Give the preparation type.
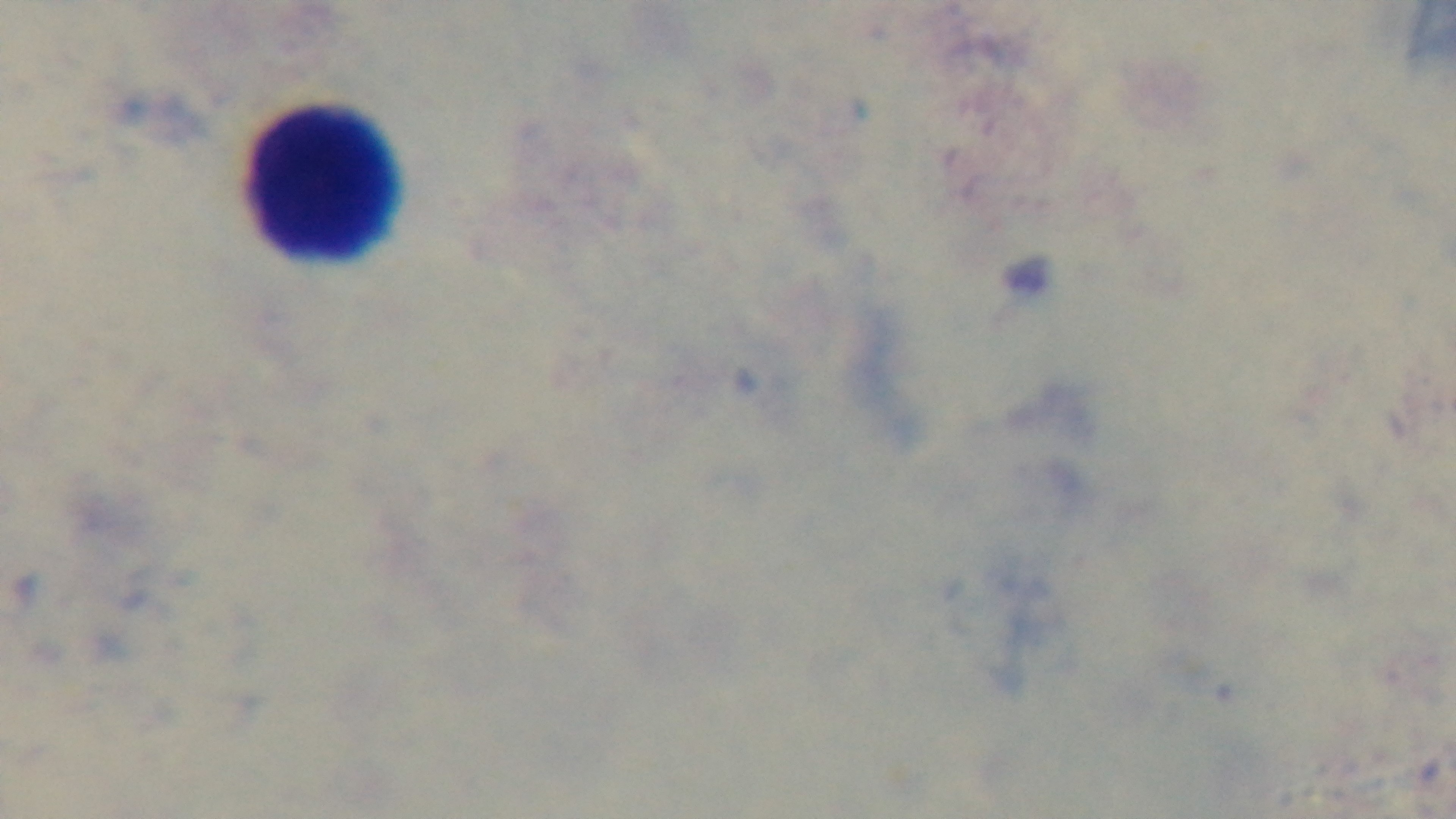
Thick.

Summary:
  - Capture: mounted 4K digital camera
  - Malaria status: uninfected
  - Field of view: one from the slide
  - Stain: Giemsa
  - Objective: 100x oil immersion
  - Modality: light microscopy